Identify the blood parasite species.
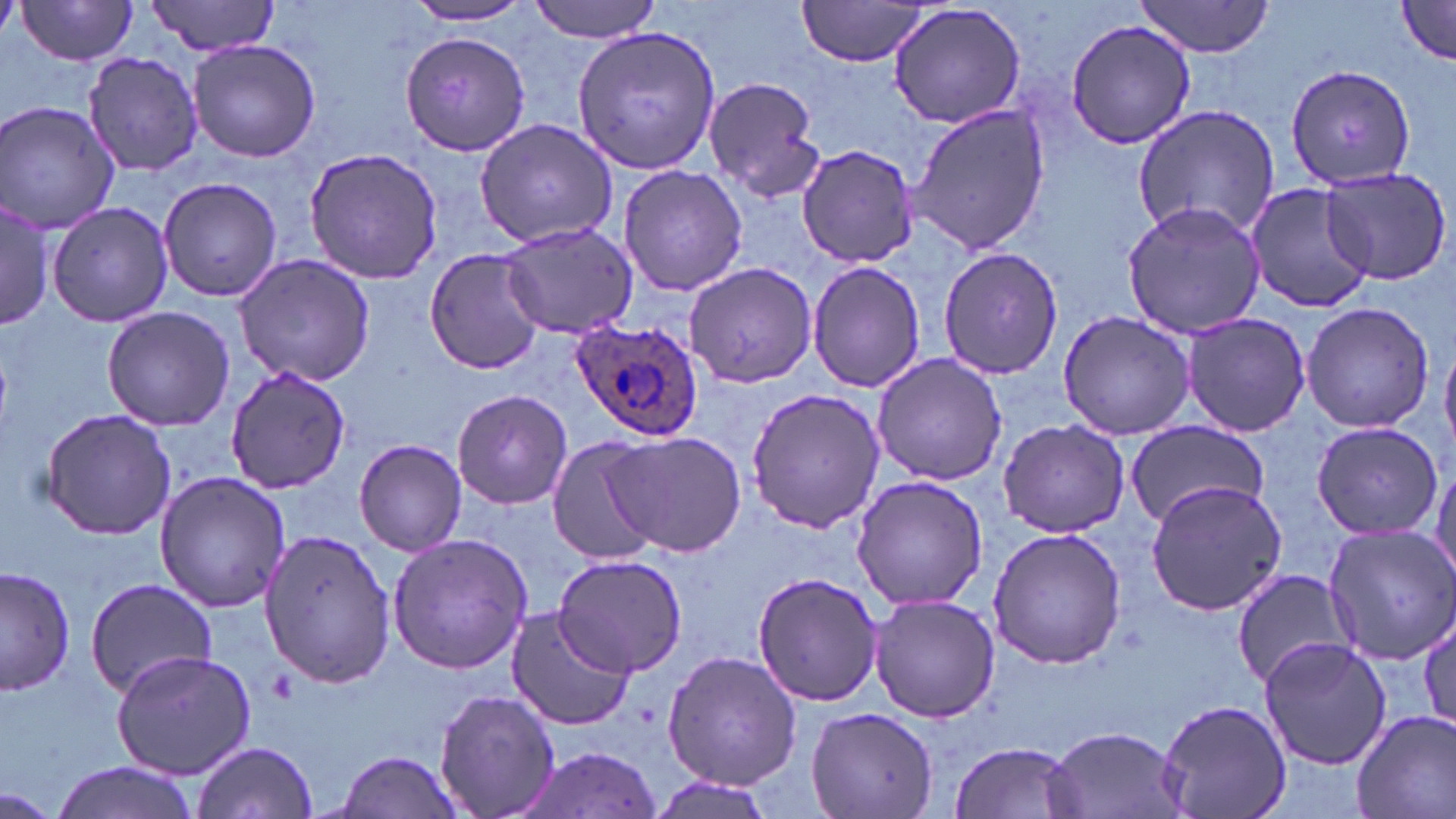
Plasmodium ovale.

Approximate bounding boxes as named x1/y1/x2/y2 corners in pixels. Uninfected red blood cell locations: (x1=146, y1=0, x2=282, y2=57), (x1=529, y1=0, x2=664, y2=42), (x1=794, y1=0, x2=940, y2=68), (x1=1133, y1=0, x2=1279, y2=58), (x1=15, y1=1, x2=142, y2=65), (x1=1393, y1=1, x2=1456, y2=68), (x1=405, y1=3, x2=538, y2=25), (x1=885, y1=3, x2=1029, y2=132), (x1=1064, y1=19, x2=1199, y2=150), (x1=572, y1=24, x2=721, y2=174), (x1=401, y1=29, x2=531, y2=156), (x1=187, y1=38, x2=322, y2=164), (x1=80, y1=51, x2=203, y2=176), (x1=1286, y1=64, x2=1418, y2=189), (x1=702, y1=75, x2=825, y2=203), (x1=0, y1=100, x2=121, y2=235), (x1=904, y1=102, x2=1050, y2=256), (x1=1133, y1=104, x2=1282, y2=244), (x1=474, y1=116, x2=621, y2=248), (x1=798, y1=144, x2=918, y2=269), (x1=303, y1=147, x2=445, y2=283), (x1=617, y1=163, x2=748, y2=298), (x1=1319, y1=168, x2=1453, y2=285), (x1=158, y1=176, x2=283, y2=301), (x1=1244, y1=181, x2=1373, y2=314), (x1=0, y1=197, x2=53, y2=333), (x1=47, y1=199, x2=176, y2=327), (x1=1121, y1=201, x2=1266, y2=338), (x1=501, y1=221, x2=639, y2=340), (x1=937, y1=245, x2=1063, y2=381), (x1=424, y1=247, x2=549, y2=374), (x1=231, y1=252, x2=378, y2=387), (x1=806, y1=259, x2=926, y2=394), (x1=685, y1=264, x2=817, y2=389), (x1=1300, y1=301, x2=1435, y2=432), (x1=101, y1=305, x2=235, y2=431), (x1=1057, y1=310, x2=1196, y2=440), (x1=1180, y1=312, x2=1311, y2=437), (x1=1441, y1=339, x2=1456, y2=450), (x1=870, y1=353, x2=1007, y2=486), (x1=225, y1=367, x2=352, y2=494), (x1=745, y1=385, x2=885, y2=534), (x1=452, y1=388, x2=573, y2=508), (x1=40, y1=408, x2=177, y2=540), (x1=1123, y1=418, x2=1268, y2=529), (x1=996, y1=419, x2=1131, y2=537), (x1=1309, y1=421, x2=1442, y2=538), (x1=606, y1=430, x2=745, y2=558), (x1=545, y1=434, x2=665, y2=565), (x1=356, y1=437, x2=468, y2=557), (x1=1430, y1=456, x2=1456, y2=581), (x1=155, y1=471, x2=292, y2=614), (x1=850, y1=475, x2=989, y2=610), (x1=1142, y1=480, x2=1288, y2=614), (x1=1322, y1=523, x2=1456, y2=663), (x1=988, y1=527, x2=1127, y2=670), (x1=257, y1=529, x2=397, y2=686), (x1=386, y1=533, x2=533, y2=674), (x1=552, y1=553, x2=689, y2=677), (x1=1, y1=564, x2=76, y2=697), (x1=750, y1=570, x2=883, y2=707), (x1=1231, y1=570, x2=1356, y2=688), (x1=83, y1=578, x2=219, y2=698), (x1=868, y1=592, x2=1000, y2=722), (x1=503, y1=607, x2=636, y2=732), (x1=1416, y1=611, x2=1454, y2=737), (x1=1258, y1=636, x2=1392, y2=770), (x1=661, y1=649, x2=803, y2=790), (x1=112, y1=650, x2=257, y2=778), (x1=433, y1=685, x2=559, y2=819), (x1=1158, y1=697, x2=1291, y2=819), (x1=805, y1=706, x2=939, y2=819), (x1=1350, y1=707, x2=1456, y2=819), (x1=1045, y1=726, x2=1188, y2=819), (x1=190, y1=739, x2=319, y2=819), (x1=949, y1=739, x2=1087, y2=819), (x1=517, y1=746, x2=666, y2=818), (x1=332, y1=749, x2=467, y2=819), (x1=48, y1=761, x2=201, y2=819), (x1=3, y1=788, x2=57, y2=816). Plasmodium ovale-infected red blood cell locations: (x1=571, y1=320, x2=705, y2=443). One field of a larger specimen. Optical microscopy. Thin blood smear. May-Grünwald-Giemsa stain. 1000x magnification. Image is 1456×819 pixels.